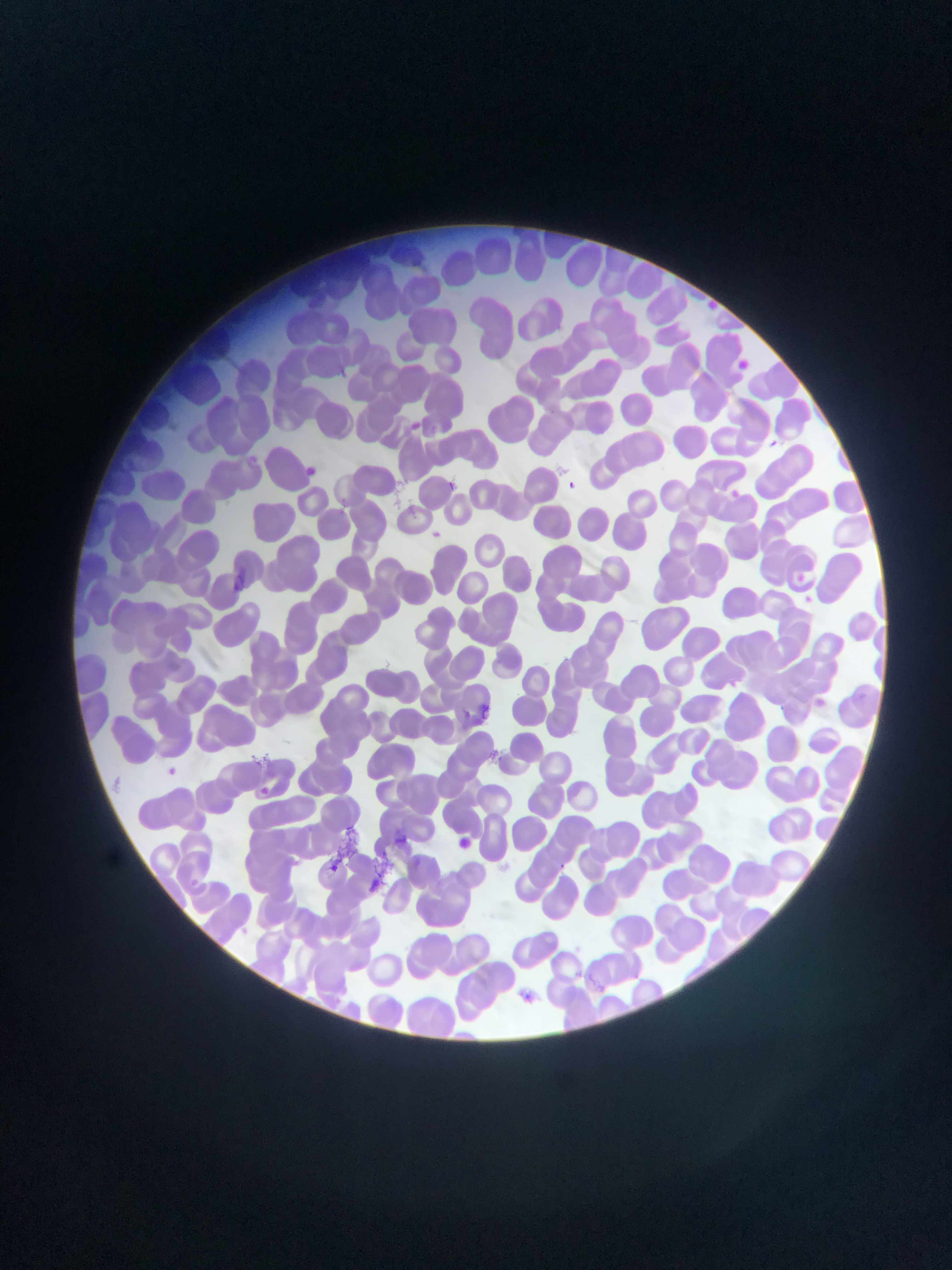

Approximate bounding boxes as left top right bottom in pixels.
Summary:
  - Artifact (stain precipitate or debris) locations: 366 833 418 892
  - Plasmodium parasite locations: 733 358 755 376; 409 420 434 437; 767 437 782 450; 300 464 324 479; 562 477 580 494; 448 478 464 504; 729 488 742 500; 792 571 807 585; 474 702 492 720; 160 762 183 783; 253 782 275 802; 450 836 475 856; 558 858 575 873; 322 860 344 879; 515 987 538 1007
  - Capture: mobile-phone photograph through a microscope
  - Field of view: single
  - Country: Ghana
  - Preparation: thin blood film
  - Image size: 952×1270 pixels